State the blood parasite species.
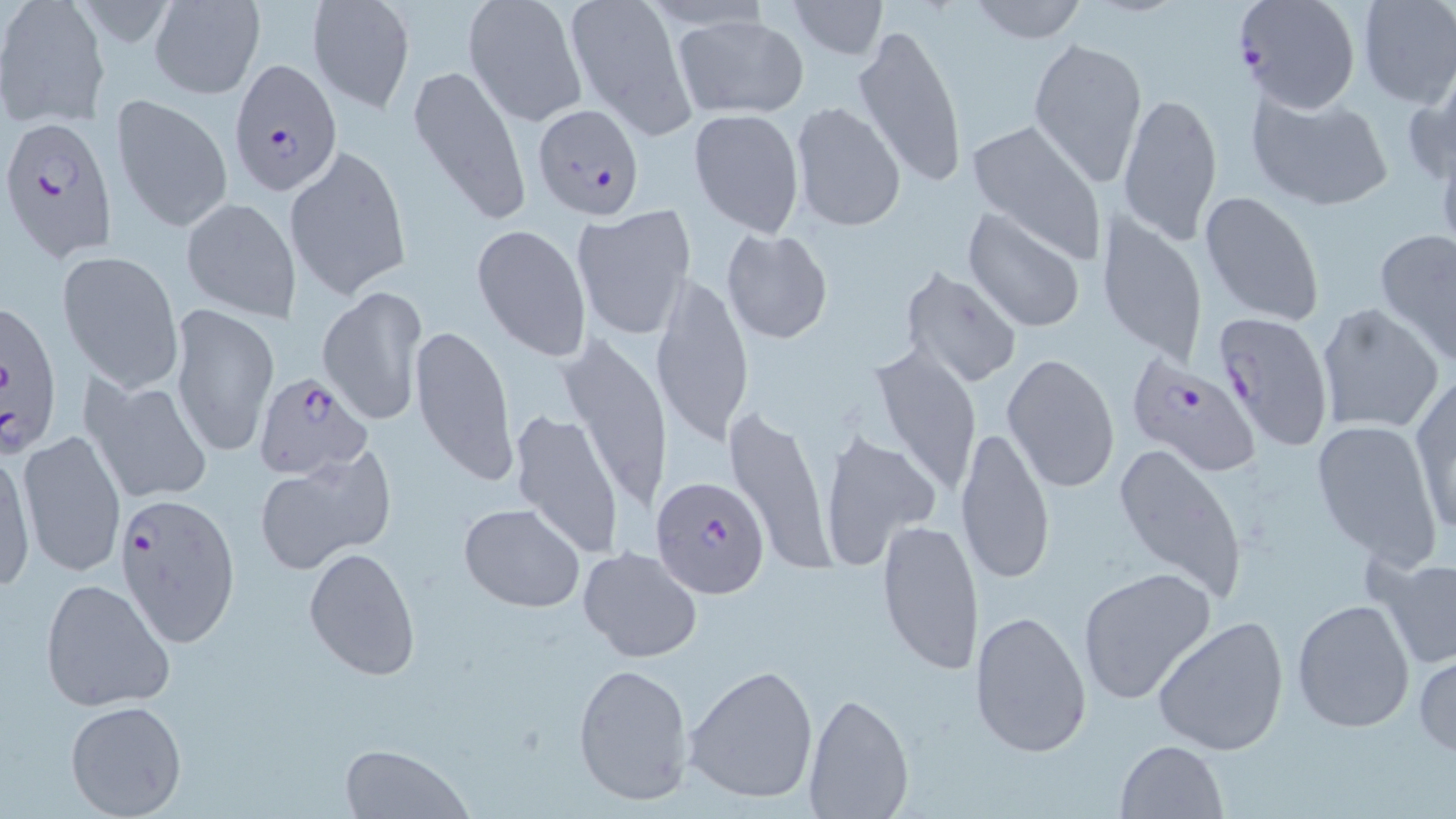
Plasmodium falciparum.

stain = May-Grünwald-Giemsa
modality = optical microscopy
Plasmodium falciparum-infected red blood cell locations = approximate bounding boxes as (x1,y1)-(x2,y2) corner pairs in pixels: (1235,0)-(1362,114), (228,59)-(342,195), (532,101)-(645,221), (2,117)-(118,264), (1,295)-(65,461), (1212,310)-(1332,454), (1124,355)-(1260,473), (254,372)-(373,479), (652,473)-(772,599), (112,490)-(241,647)
image size = 1456×819 pixels
uninfected red blood cell locations = approximate bounding boxes as (x1,y1)-(x2,y2) corner pairs in pixels: (148,0)-(265,98), (305,0)-(416,114), (563,0)-(693,136), (787,0)-(888,60), (798,0)-(928,92), (965,0)-(1091,44), (1355,0)-(1456,108), (461,1)-(586,127), (1,3)-(110,128), (672,14)-(809,121), (851,22)-(969,190), (1028,36)-(1147,189), (1401,62)-(1455,191), (407,63)-(531,229), (1117,89)-(1224,245), (1246,90)-(1395,212), (109,93)-(233,234), (789,103)-(906,232), (688,108)-(805,237), (966,119)-(1106,263), (286,145)-(413,302), (1199,189)-(1326,327), (181,197)-(300,324), (571,204)-(697,340), (962,208)-(1087,334), (1095,209)-(1208,366), (472,222)-(592,363), (721,227)-(834,345), (1375,228)-(1456,361), (57,250)-(184,390), (901,268)-(1022,388), (651,274)-(752,450), (317,286)-(428,427), (169,301)-(278,458), (1315,303)-(1444,434), (411,322)-(516,487), (554,331)-(674,516), (865,345)-(986,495), (1002,352)-(1121,494), (1410,374)-(1456,536), (83,375)-(215,505), (725,408)-(834,575), (507,409)-(625,559), (1310,419)-(1443,565), (954,426)-(1056,591), (17,428)-(127,577), (818,429)-(941,571), (1113,441)-(1248,603), (1,449)-(36,592), (252,452)-(393,576), (458,502)-(585,612), (876,516)-(984,675), (302,546)-(421,681), (577,546)-(703,664), (1370,554)-(1456,672), (1078,566)-(1219,706), (39,576)-(175,715), (1292,598)-(1417,734), (970,608)-(1093,760), (1153,615)-(1290,756), (1413,652)-(1456,758), (572,661)-(694,806), (683,664)-(818,805), (803,693)-(912,818), (65,701)-(189,819), (1115,739)-(1230,819), (336,742)-(473,819)
preparation = thin blood film
field of view = single
magnification = 1000x